Assess the morphology of the erythrocytes.
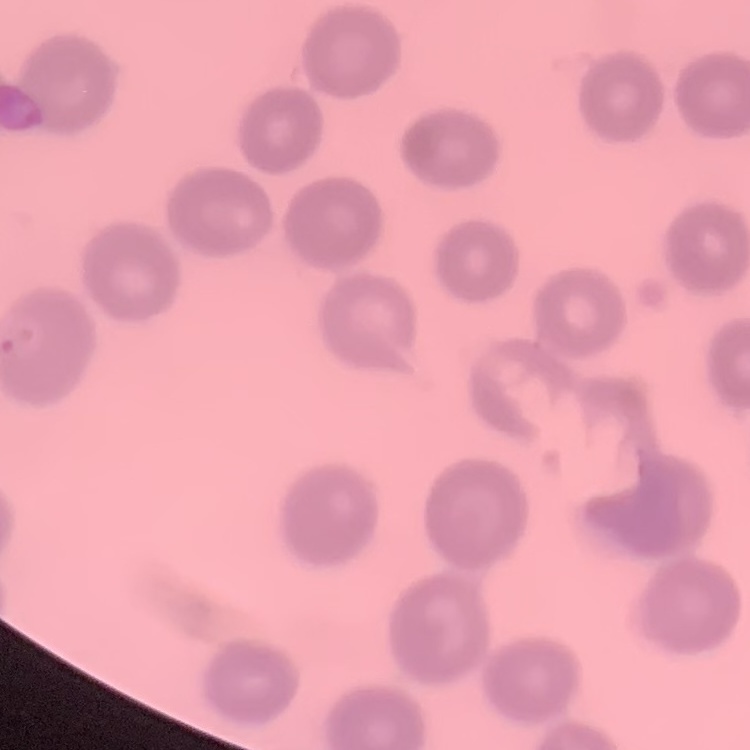
No rouleaux formation.

stain = Field's or Giemsa
preparation = thin blood smear
image type = one tile cut from a larger photomicrograph